Assess the morphology of the red blood cells.
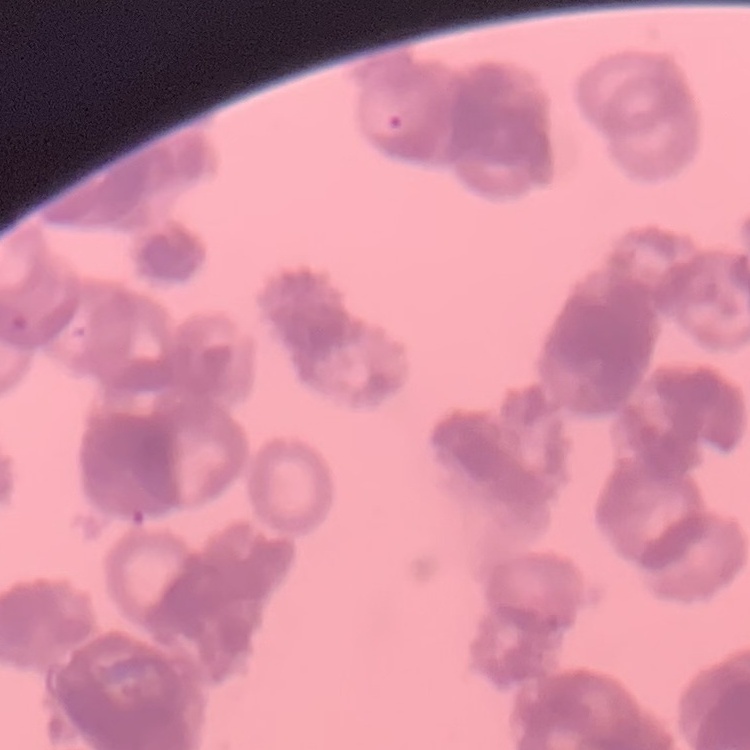
Rouleaux formation.

Stained with either Field's or Giemsa. Square crop of a larger photomicrograph. Thin peripheral smear.